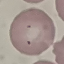

Summary:
  - Malaria status: parasitized
  - Capture: smartphone camera at the microscope eyepiece
  - Image type: automatically extracted cell patch, resized to 64 × 64 pixels
  - Preparation: thin smear
  - Stain: Giemsa